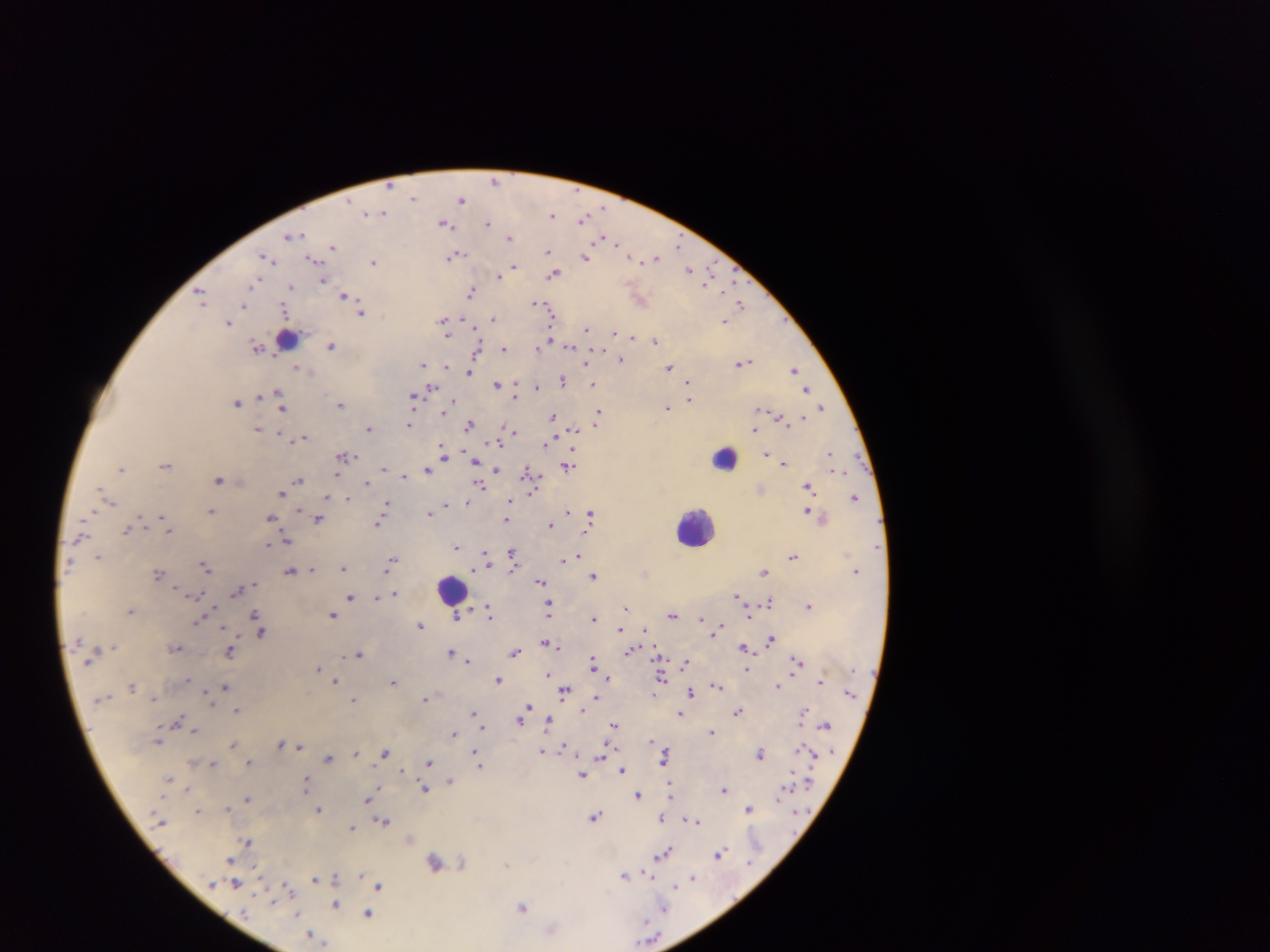 Approximate centers as [x, y] in pixels. Leukocyte locations: [283, 337], [722, 456], [695, 526], [451, 590]. Plasmodium parasite locations: [495, 179], [413, 198], [461, 199], [382, 212], [552, 214], [583, 218], [444, 223], [487, 223], [291, 235], [509, 237], [620, 245], [678, 245], [333, 246], [549, 251], [454, 255], [586, 256], [630, 256], [656, 257], [266, 258], [314, 258], [551, 258], [374, 262], [513, 266], [691, 270], [554, 273], [499, 275], [324, 281], [708, 283], [254, 284], [291, 287], [471, 293], [202, 296], [344, 296], [536, 303], [245, 305], [741, 305], [542, 307], [362, 312], [493, 318], [443, 320], [724, 321], [229, 322], [587, 330], [614, 332], [630, 336], [655, 340], [332, 346], [570, 346], [258, 347], [539, 347], [503, 348], [476, 353], [621, 359], [743, 362], [423, 364], [473, 364], [447, 367], [299, 368], [669, 368], [794, 369], [470, 371], [563, 380], [593, 383], [497, 384], [689, 384], [515, 386], [537, 386], [432, 388], [807, 390], [515, 395], [280, 396], [413, 398], [690, 399], [454, 401], [236, 402], [281, 404], [341, 404], [667, 408], [822, 408], [599, 413], [553, 417], [409, 424], [596, 424], [469, 425], [258, 429], [369, 429], [573, 430], [754, 431], [511, 432], [301, 439], [497, 441], [547, 443], [443, 454], [766, 454], [832, 456], [344, 457], [474, 461], [785, 463], [166, 465], [568, 466], [122, 468], [497, 470], [386, 471], [427, 471], [529, 473], [404, 476], [218, 479], [299, 480], [366, 482], [480, 485], [808, 487], [105, 494], [281, 494], [329, 497], [855, 497], [347, 498], [107, 499], [466, 502], [385, 505], [446, 505], [509, 505], [212, 510], [807, 511], [430, 512], [567, 512], [589, 515], [271, 518], [507, 518], [318, 519], [165, 523], [378, 523], [550, 525], [168, 528], [127, 530], [286, 541], [456, 548], [512, 555], [792, 555], [486, 556], [98, 557], [574, 557], [392, 561], [206, 566], [343, 567], [312, 569], [290, 571], [764, 571], [158, 574], [594, 575], [540, 582], [238, 590], [395, 594], [738, 596], [350, 598], [376, 598], [769, 601], [549, 606], [809, 606], [626, 608], [131, 611], [490, 614], [255, 615], [333, 615], [672, 615], [457, 617], [595, 618], [701, 619], [199, 621], [420, 625], [644, 629], [620, 630], [717, 631], [261, 632], [770, 640], [547, 643], [743, 647], [175, 648], [629, 651], [230, 652], [451, 652], [515, 652], [358, 653], [468, 661], [797, 661], [684, 663], [593, 665], [318, 669], [746, 669], [549, 674], [608, 678], [660, 678], [499, 680], [335, 681], [820, 681], [393, 682], [133, 686], [717, 686], [778, 686], [225, 687], [564, 691], [690, 692], [596, 698], [425, 699], [354, 701], [525, 709], [237, 710], [738, 711], [803, 712], [473, 713], [679, 713], [521, 718], [549, 721], [179, 722], [614, 725], [826, 726], [482, 727], [196, 732], [713, 732], [454, 734], [158, 740], [233, 744], [282, 744], [298, 747], [564, 747], [543, 750], [356, 753], [385, 753], [761, 753], [603, 754], [476, 755], [665, 757], [329, 758], [250, 762], [212, 763], [429, 763], [478, 763], [623, 770], [582, 775], [169, 779], [451, 781], [305, 784], [187, 789], [425, 790], [724, 790], [670, 793], [638, 794], [247, 798], [368, 799], [228, 808], [749, 808], [197, 810], [319, 810], [595, 816], [662, 817], [695, 821], [385, 822], [352, 828], [247, 842], [720, 853], [663, 854], [230, 860], [435, 862], [462, 862], [625, 875], [692, 877], [315, 878], [335, 878], [235, 884], [379, 885], [287, 887], [336, 904], [522, 907], [665, 909], [368, 915], [552, 929], [312, 935], [318, 939]. Thick blood film. Photographed through a microscope with a mobile-phone camera. Collected in Ghana. One field of view. Image is 1270×952 pixels.